Locate every Plasmodium parasite by life-cycle stage, and every leukocyte.
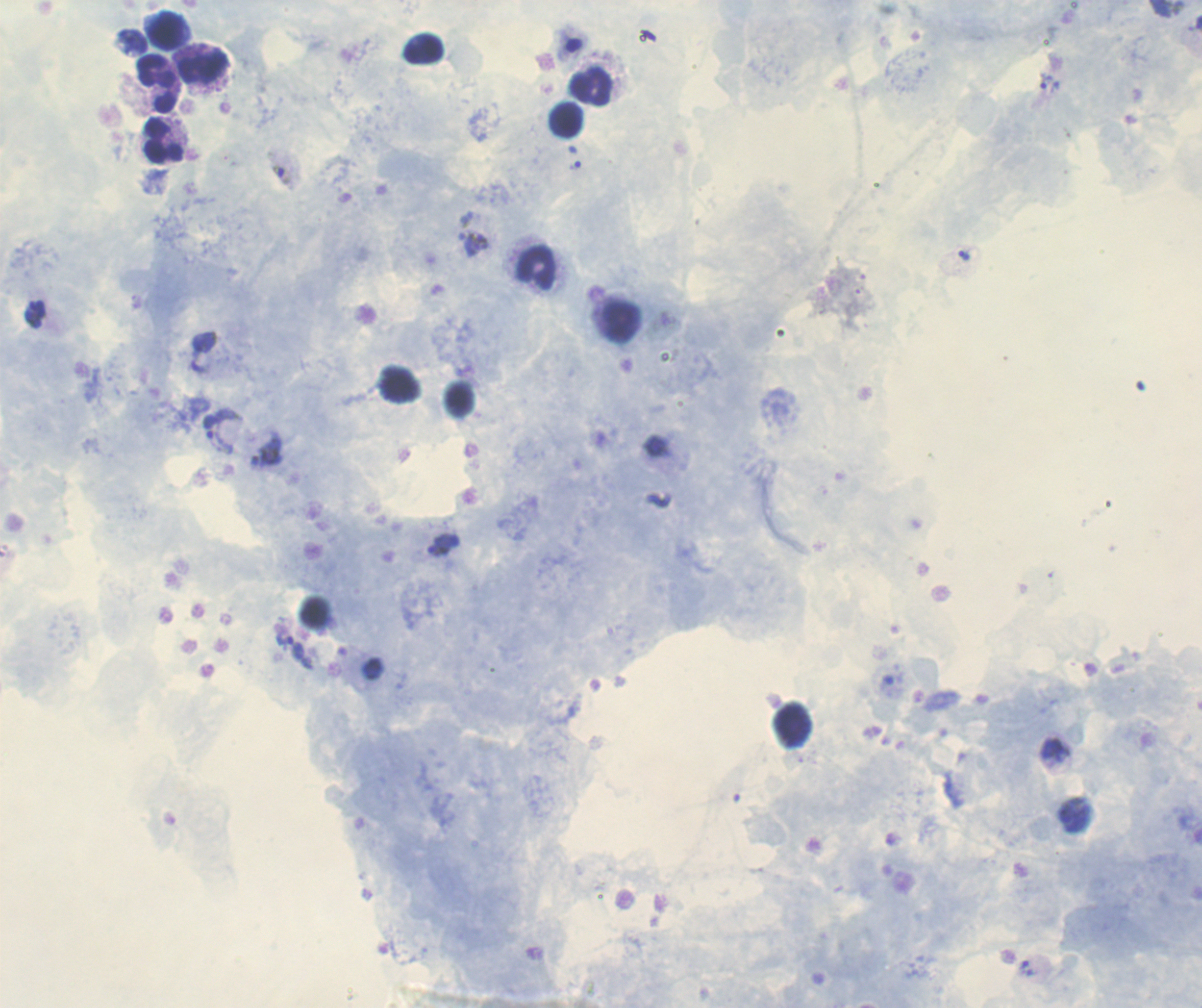

Approximate object centers, in pixels from the top-left corner.
Trophozoites: (x=131, y=42), (x=1045, y=81), (x=575, y=165), (x=474, y=244), (x=964, y=256), (x=35, y=314), (x=205, y=341), (x=210, y=424), (x=439, y=544), (x=295, y=647), (x=1055, y=749), (x=1026, y=967).
Gametocytes: (x=282, y=175).
No schizont forms observed.
Leukocytes: (x=168, y=29), (x=423, y=49), (x=205, y=65), (x=157, y=84), (x=591, y=87), (x=568, y=120), (x=162, y=141), (x=537, y=269), (x=621, y=321).

Romanowsky stain. Previously used in a real diagnosis. 100x magnification. Thick blood smear. Coloration quality: good. One field from this slide. Background quality: good. Image is 1202×1008 pixels.